Assess this cell for malaria.
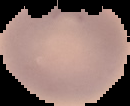

Uninfected.

Summary:
  - Preparation: thin blood smear
  - Image size: 130×106 pixels
  - Image type: segmented cell region with the area outside set to black